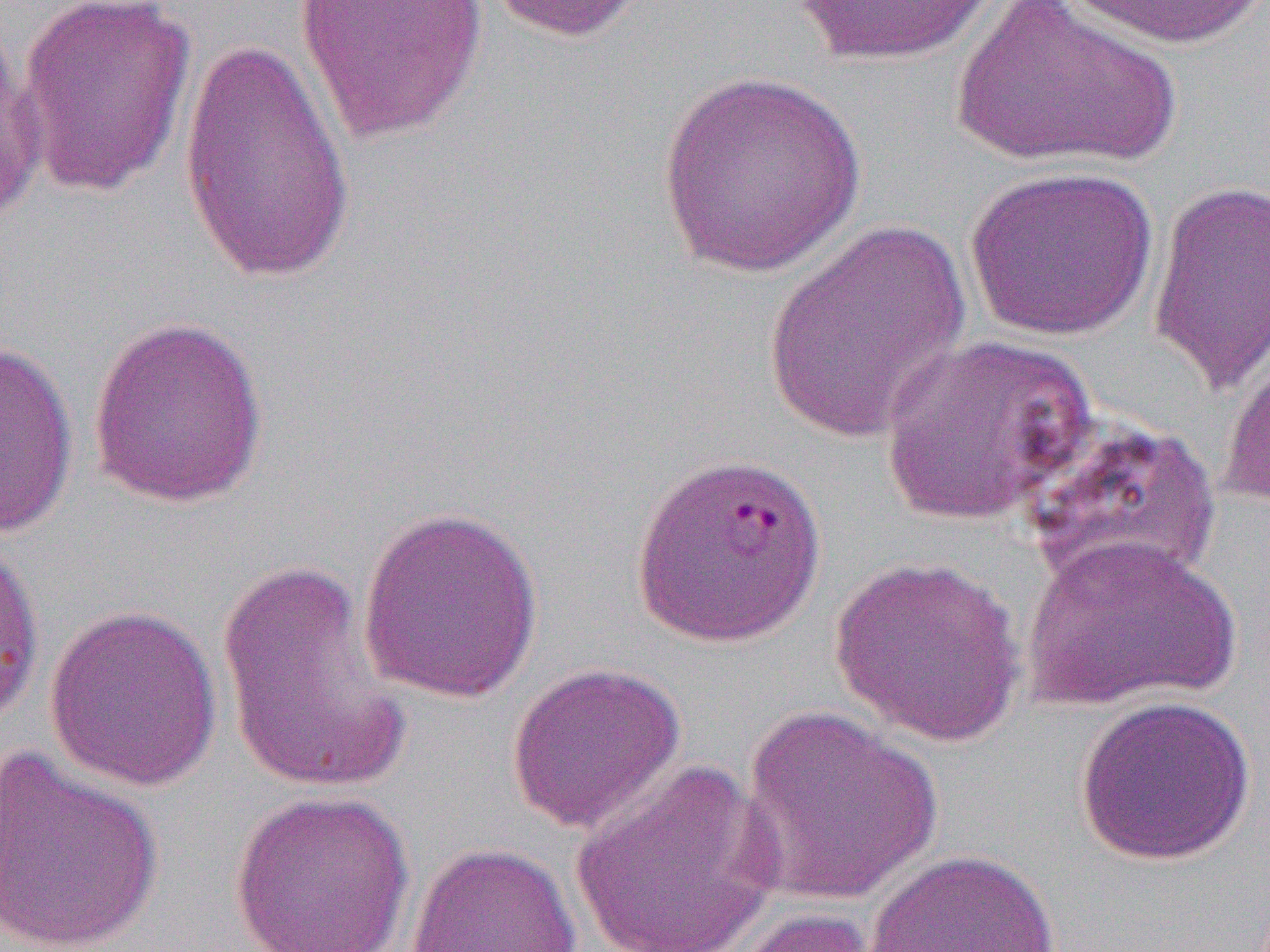
slide-level diagnosis = Plasmodium falciparum
preparation = thin blood film
uninfected red blood cell locations = approximate bounding boxes as [x1, y1, x2, y2] in pixels: [12, 0, 198, 199], [293, 0, 488, 143], [481, 0, 655, 44], [785, 0, 1005, 67], [948, 0, 1184, 172], [1064, 1, 1264, 49], [1, 12, 46, 228], [178, 32, 358, 287], [658, 71, 866, 277], [964, 165, 1160, 341], [1146, 179, 1269, 396], [763, 219, 971, 445], [87, 313, 270, 510], [879, 333, 1096, 526], [0, 335, 81, 542], [1219, 336, 1270, 515], [1020, 413, 1222, 593], [355, 505, 545, 706], [1021, 532, 1241, 712], [0, 536, 45, 731], [829, 554, 1027, 746], [217, 558, 414, 795], [43, 603, 222, 792], [504, 662, 687, 835], [1074, 695, 1256, 867], [738, 704, 944, 906], [0, 748, 165, 952], [567, 760, 786, 952], [228, 789, 416, 951], [404, 841, 582, 951], [864, 848, 1061, 952], [716, 907, 894, 952]
field of view = single
magnification = 1000x
image size = 1270×952 pixels
modality = optical microscopy
Plasmodium falciparum-infected red blood cell locations = approximate bounding boxes as [x1, y1, x2, y2] in pixels: [629, 451, 827, 648]